Outline each blood parasite and name the species.
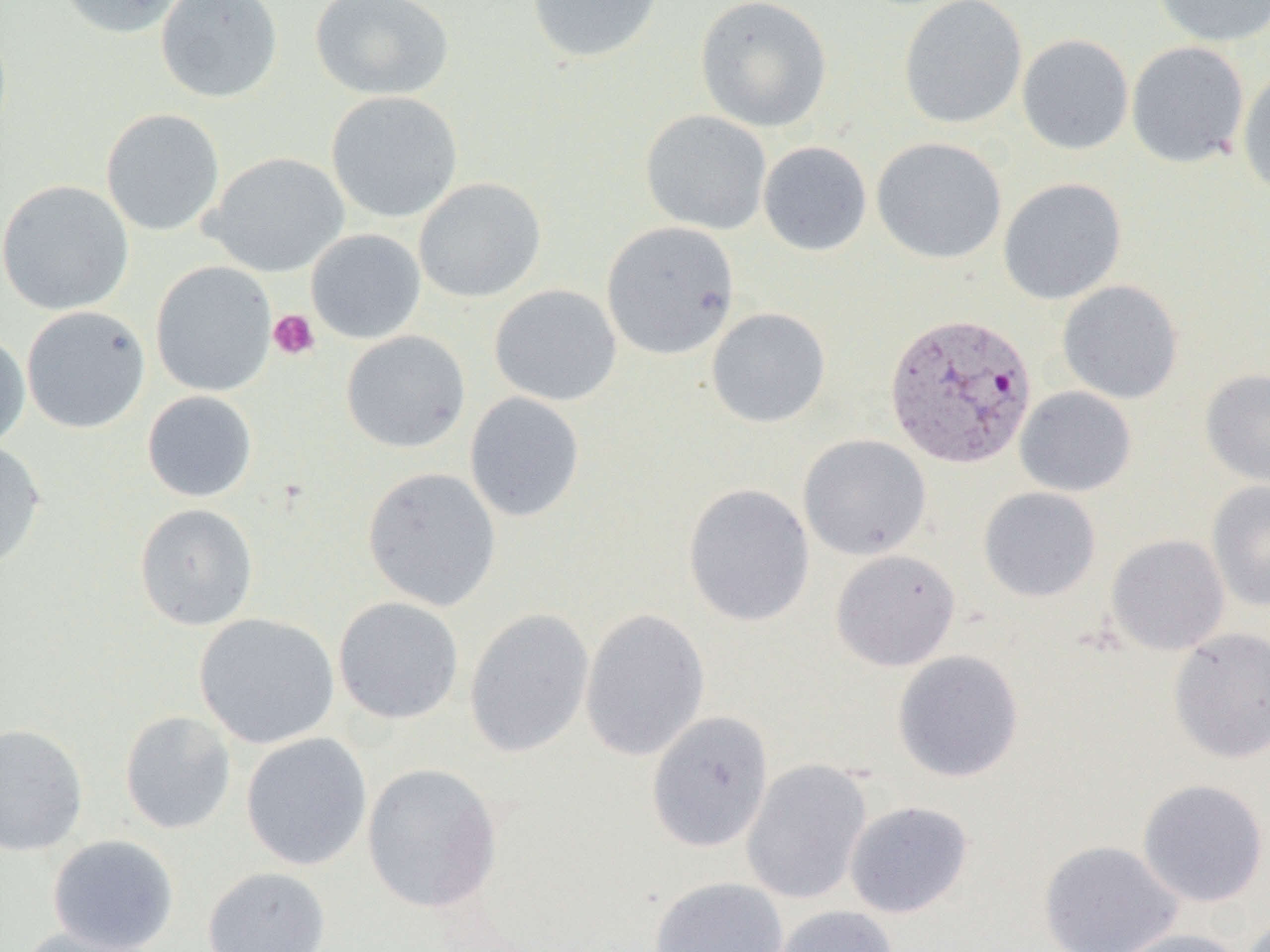
Approximate bounding boxes as [x1, y1, x2, y2] in pixels.
Plasmodium vivax-infected red blood cells: [884, 311, 1038, 469].
No Plasmodium falciparum, Plasmodium ovale, Plasmodium malariae, Babesia divergens, or Trypanosoma brucei observed.

slide_level_diagnosis: Plasmodium vivax
preparation: thin blood film
image_size: 1270×952 pixels
uninfected_red_blood_cell_locations: 'approximate bounding boxes as [x1, y1, x2, y2] in pixels: [54, 0, 189, 39], [156, 0, 283, 103], [309, 0, 454, 101], [527, 0, 663, 64], [694, 0, 833, 133], [898, 0, 1028, 129], [1150, 0, 1270, 47], [1017, 34, 1134, 155], [1126, 41, 1249, 168], [1237, 66, 1270, 196], [326, 91, 463, 223], [100, 108, 225, 236], [640, 110, 772, 235], [871, 137, 1007, 264], [758, 141, 872, 257], [203, 152, 349, 277], [413, 177, 547, 303], [998, 177, 1127, 305], [0, 180, 134, 316], [601, 221, 740, 360], [306, 229, 426, 344], [150, 262, 277, 397], [1057, 280, 1183, 404], [489, 285, 622, 406], [21, 305, 151, 433], [706, 307, 831, 428], [0, 331, 30, 450], [341, 331, 471, 453], [1200, 369, 1270, 489], [1015, 386, 1137, 497], [142, 390, 257, 502], [464, 392, 585, 522], [797, 434, 931, 560], [0, 439, 47, 571], [362, 466, 502, 611], [1207, 480, 1270, 612], [682, 482, 816, 627], [978, 487, 1101, 602], [133, 503, 259, 631], [1106, 533, 1230, 655], [830, 549, 960, 671], [333, 596, 464, 724], [464, 608, 595, 758], [580, 608, 710, 762], [193, 613, 340, 748], [1168, 626, 1270, 764], [892, 650, 1024, 783], [119, 710, 237, 835], [646, 710, 774, 853], [0, 722, 89, 856], [240, 732, 373, 871], [741, 758, 872, 904], [361, 762, 503, 914], [1137, 778, 1269, 907], [845, 800, 974, 918], [46, 834, 180, 952], [1038, 839, 1184, 952], [201, 866, 331, 952], [648, 876, 788, 952], [770, 905, 899, 952], [1241, 913, 1270, 952], [15, 926, 161, 952], [1106, 928, 1250, 952]'
magnification: 1000x
platelet_locations: 'approximate bounding boxes as [x1, y1, x2, y2] in pixels: [268, 308, 321, 361]'
field_of_view: single
modality: optical microscopy